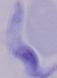

A trypanosome is seen. 1000x magnification. Micrograph.